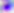
Summary:
  - Magnification: 400x
  - Identification: Toxoplasma gondii
  - Modality: micrograph